Identify the parasite.
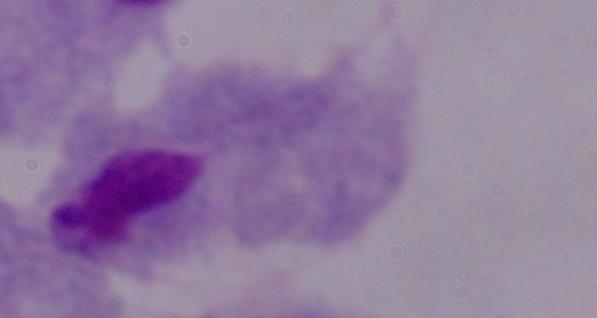
A trichomonad.

Summary:
  - Modality: micrograph
  - Magnification: 1000x